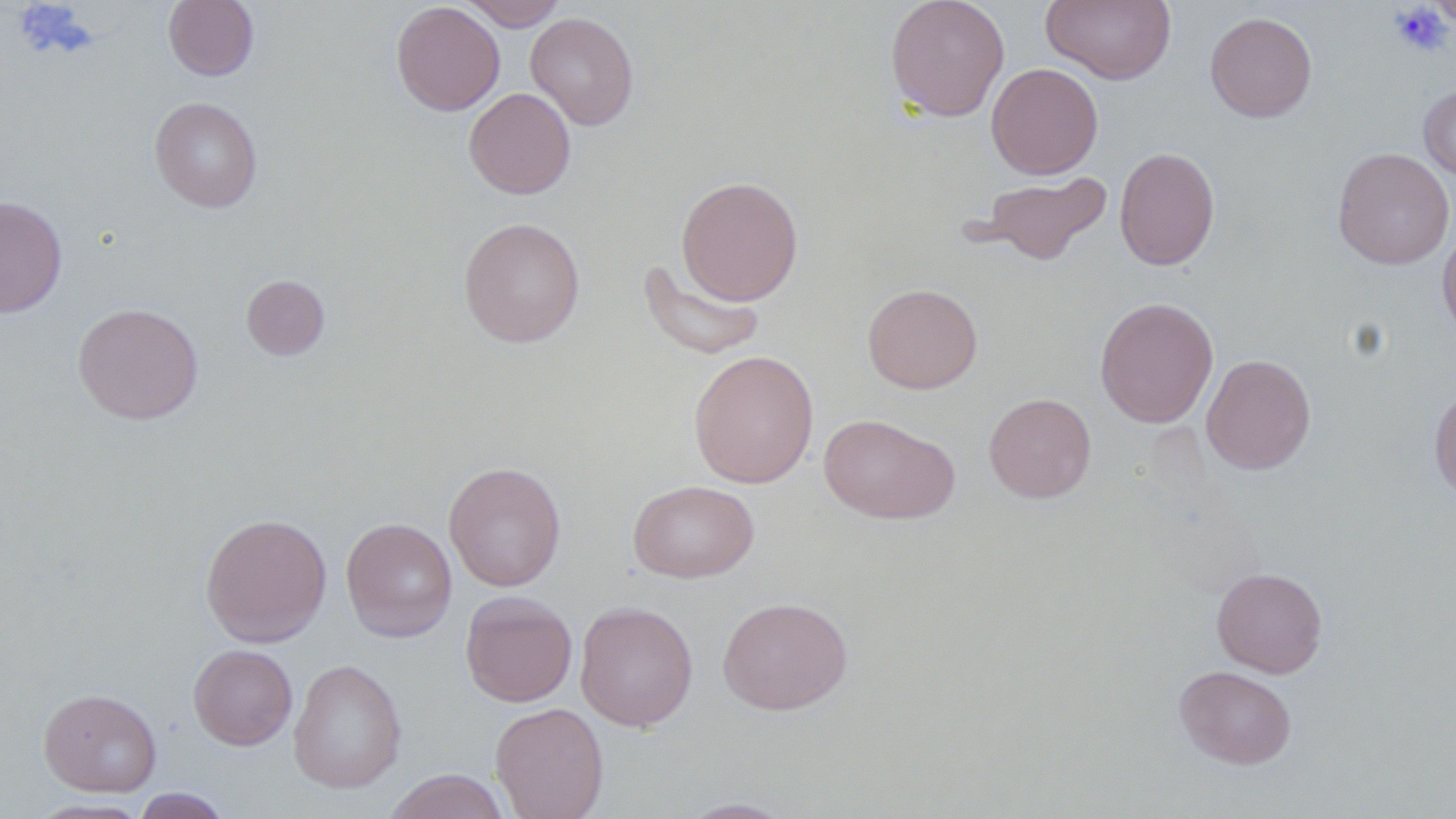
Summary:
  - Coordinate format: approximate bounding boxes as named x1/y1/x2/y2 corners in pixels
  - Platelet locations: (x1=1389, y1=3, x2=1453, y2=57)
  - Uninfected red blood cell locations: (x1=164, y1=0, x2=259, y2=81), (x1=459, y1=0, x2=567, y2=30), (x1=885, y1=0, x2=1010, y2=122), (x1=1041, y1=0, x2=1177, y2=85), (x1=1428, y1=0, x2=1456, y2=30), (x1=391, y1=2, x2=505, y2=116), (x1=1205, y1=11, x2=1317, y2=123), (x1=525, y1=12, x2=639, y2=130), (x1=986, y1=62, x2=1103, y2=179), (x1=1418, y1=84, x2=1456, y2=183), (x1=464, y1=87, x2=576, y2=199), (x1=149, y1=96, x2=263, y2=213), (x1=1114, y1=147, x2=1220, y2=271), (x1=1332, y1=147, x2=1454, y2=269), (x1=975, y1=171, x2=1111, y2=266), (x1=676, y1=175, x2=804, y2=306), (x1=0, y1=196, x2=68, y2=318), (x1=458, y1=216, x2=585, y2=348), (x1=1437, y1=226, x2=1456, y2=343), (x1=638, y1=257, x2=766, y2=361), (x1=241, y1=274, x2=330, y2=360), (x1=862, y1=283, x2=983, y2=394), (x1=1095, y1=297, x2=1218, y2=428), (x1=73, y1=303, x2=204, y2=424), (x1=688, y1=349, x2=819, y2=488), (x1=1201, y1=353, x2=1316, y2=475), (x1=1429, y1=386, x2=1456, y2=504), (x1=983, y1=393, x2=1096, y2=503), (x1=819, y1=412, x2=960, y2=525), (x1=444, y1=461, x2=566, y2=591), (x1=628, y1=479, x2=759, y2=583), (x1=200, y1=513, x2=332, y2=647), (x1=341, y1=517, x2=457, y2=643), (x1=1211, y1=567, x2=1328, y2=678), (x1=460, y1=591, x2=577, y2=707), (x1=717, y1=596, x2=853, y2=715), (x1=574, y1=601, x2=698, y2=731), (x1=188, y1=644, x2=298, y2=750), (x1=288, y1=658, x2=407, y2=794), (x1=1174, y1=665, x2=1297, y2=769), (x1=38, y1=688, x2=162, y2=797), (x1=490, y1=702, x2=609, y2=819), (x1=383, y1=769, x2=511, y2=819), (x1=131, y1=787, x2=232, y2=818), (x1=674, y1=797, x2=798, y2=818), (x1=27, y1=798, x2=152, y2=818)
  - Slide-level diagnosis: negative for blood parasites
  - Field of view: single
  - Magnification: 1000x
  - Image size: 1456×819 pixels
  - Preparation: thin blood film
  - Modality: optical microscopy
  - Stain: May-Grünwald-Giemsa